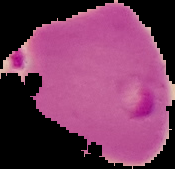

preparation = thin blood film
image size = 175×169 pixels
malaria status = parasitized
image type = segmented cell region with the area outside set to black